Classify this cell by malaria status.
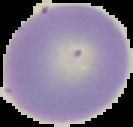

It is uninfected.

The area outside the segmented cell region is set to black. Image is 133×127 pixels. From a thin blood smear.